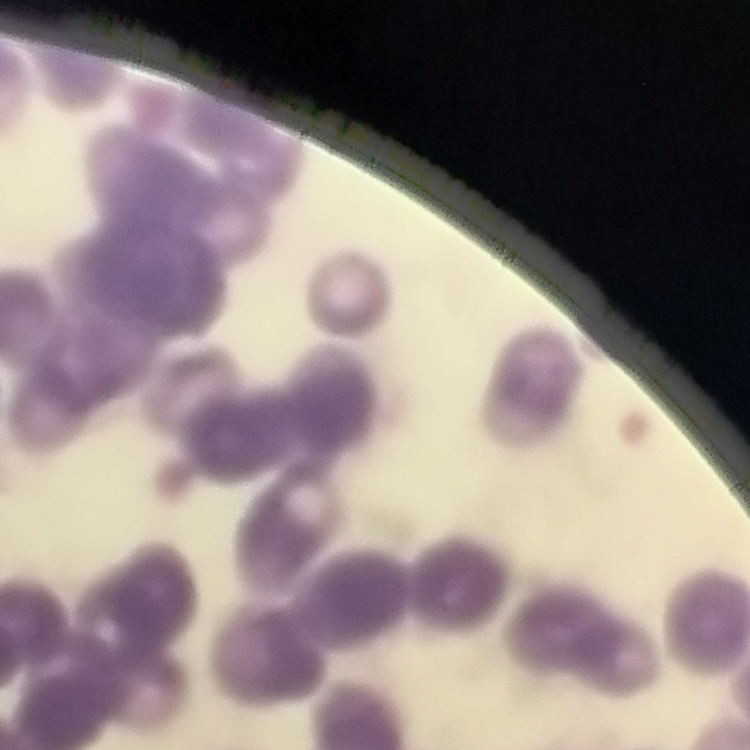

The erythrocytes exhibit rouleaux formation. Field's or Giemsa stain. Thin peripheral smear. Square crop of a larger photomicrograph.